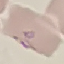

malaria status = parasitized
capture = smartphone through the microscope eyepiece
image type = automatically extracted cell patch, resized to 64 × 64 pixels
preparation = thin blood film
stain = Giemsa